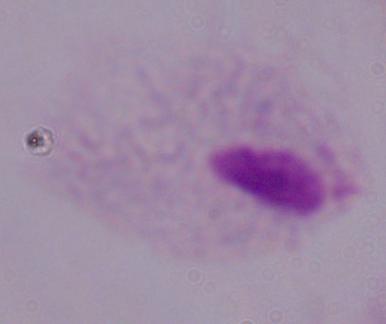
Summary:
  - Modality: photomicrograph
  - Identification: trichomonad
  - Magnification: 1000x